Locate and identify every blood parasite.
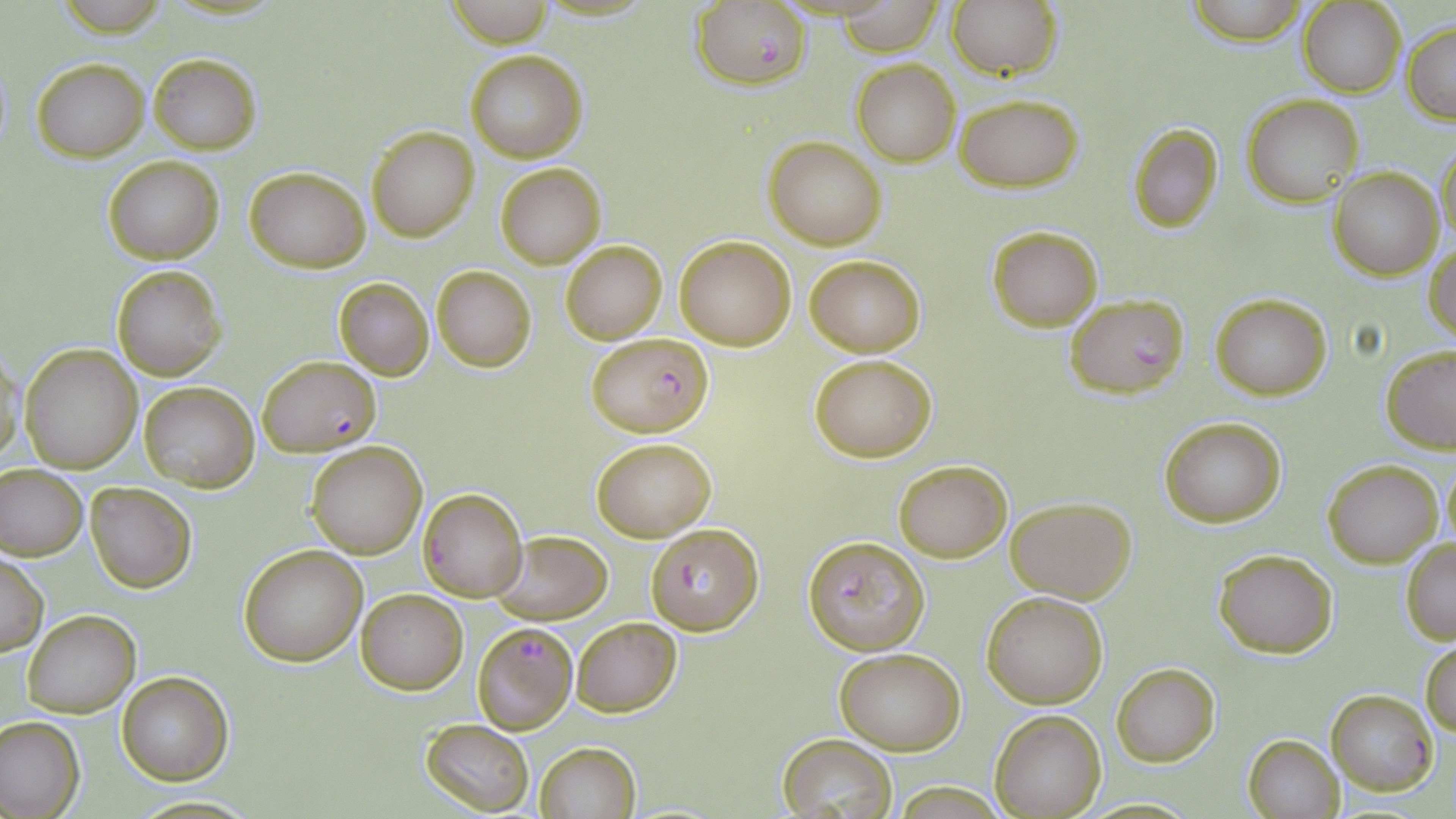

Approximate bounding boxes as (x1,y1)-(x2,y2) corner pairs in pixels.
Plasmodium falciparum-infected red blood cells: (693,1)-(812,89), (1063,291)-(1191,399), (587,332)-(715,436), (258,356)-(381,455), (419,489)-(528,601), (645,523)-(762,634), (803,534)-(930,656), (473,621)-(577,735).
No Plasmodium ovale, Plasmodium malariae, Plasmodium vivax, Babesia divergens, or Trypanosoma brucei observed.

Uninfected red blood cell locations: (441,0)-(562,47), (1182,0)-(1315,45), (837,1)-(945,56), (947,2)-(1062,80), (1300,2)-(1406,97), (1402,23)-(1456,123), (464,51)-(588,163), (148,53)-(263,153), (33,58)-(150,162), (851,59)-(961,167), (955,94)-(1084,190), (1245,95)-(1363,207), (1129,125)-(1224,231), (367,126)-(480,242), (763,136)-(888,250), (1435,145)-(1456,250), (103,155)-(224,264), (495,163)-(607,269), (246,166)-(370,272), (1329,168)-(1442,280), (986,225)-(1102,331), (675,235)-(796,350), (560,240)-(667,345), (1426,244)-(1456,341), (804,254)-(925,357), (111,264)-(227,381), (431,265)-(537,372), (334,277)-(435,380), (1210,292)-(1332,401), (1,344)-(26,469), (19,345)-(142,474), (1381,345)-(1456,454), (809,354)-(938,460), (139,382)-(258,492), (1160,417)-(1287,528), (592,435)-(717,542), (306,441)-(428,559), (1441,454)-(1455,552), (894,459)-(1011,562), (1323,460)-(1443,568), (0,466)-(88,560), (85,481)-(197,594), (1007,497)-(1136,603), (490,530)-(612,625), (1400,539)-(1456,643), (238,544)-(367,665), (1213,547)-(1339,658), (0,553)-(48,655), (355,587)-(468,695), (982,591)-(1110,709), (22,610)-(140,717), (571,617)-(682,718), (1420,641)-(1456,737), (834,647)-(966,754), (1112,663)-(1221,766), (116,672)-(232,786), (1327,689)-(1437,795), (991,709)-(1106,817), (0,716)-(85,818), (419,718)-(535,816), (775,732)-(900,817), (1242,733)-(1344,818), (534,742)-(641,819). Slide-level diagnosis: Plasmodium falciparum. 1000x magnification. May-Grünwald-Giemsa stain. Single field of view. Optical microscopy. Thin blood film. Image is 1456×819 pixels.